Outline each blood parasite and name the species.
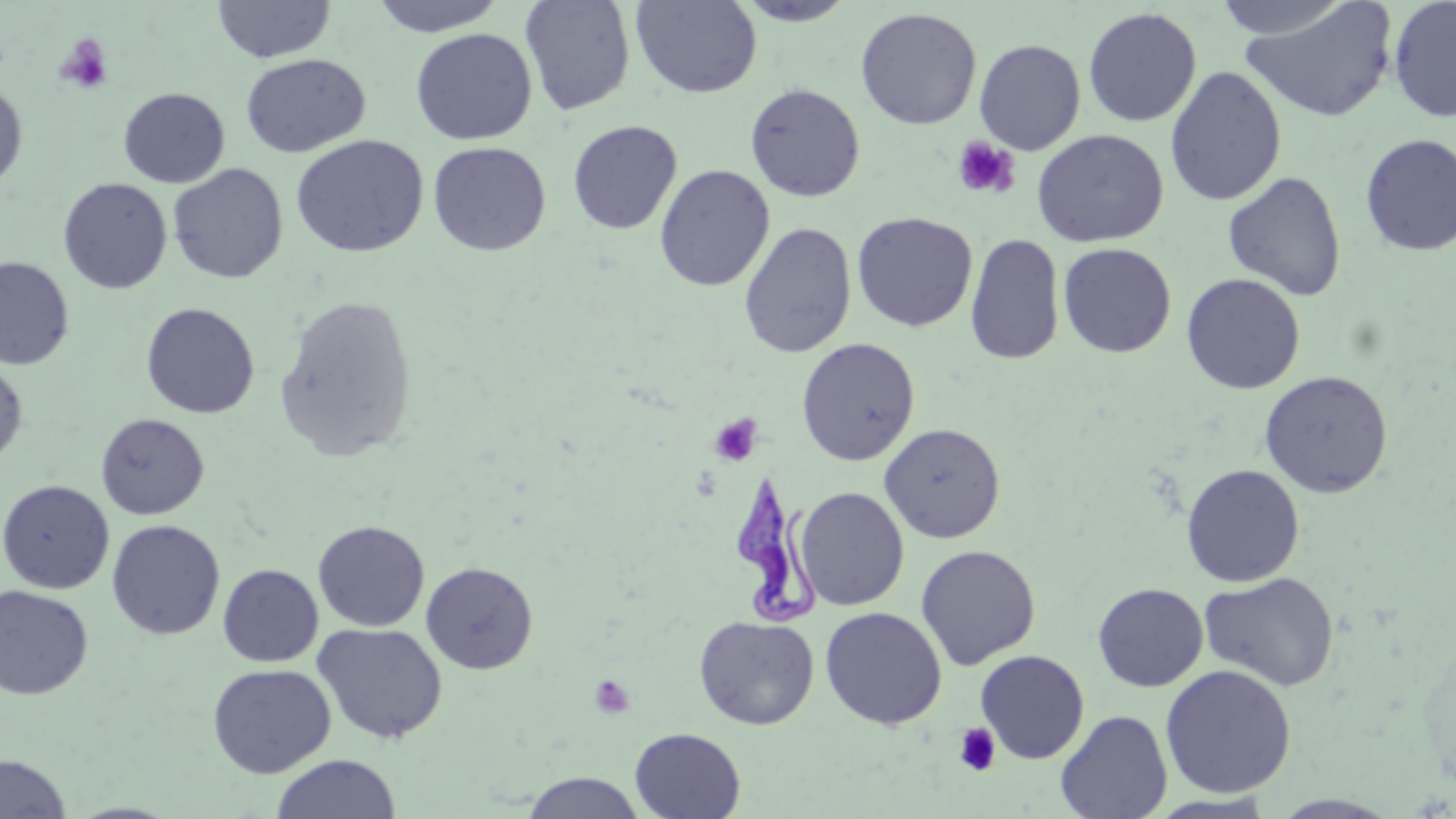
Approximate bounding boxes as (x1,y1)-(x2,y2) corner pairs in pixels.
Trypanosoma brucei: (725,475)-(826,628).
No Plasmodium falciparum, Plasmodium ovale, Plasmodium malariae, Plasmodium vivax, or Babesia divergens observed.

slide_level_diagnosis: Trypanosoma brucei
modality: light microscopy
platelet_locations: 'approximate bounding boxes as (x1,y1)-(x2,y2) corner pairs in pixels: (54,33)-(113,94), (951,136)-(1020,199), (709,414)-(762,466), (588,674)-(635,719), (953,723)-(1001,776)'
image_size: 1456×819 pixels
uninfected_red_blood_cell_locations: 'approximate bounding boxes as (x1,y1)-(x2,y2) corner pairs in pixels: (367,0)-(509,37), (519,0)-(637,116), (630,0)-(762,99), (1209,0)-(1356,41), (1387,0)-(1456,123), (212,1)-(335,63), (730,1)-(861,26), (1239,1)-(1399,123), (854,7)-(982,130), (1082,7)-(1202,127), (411,28)-(537,145), (974,39)-(1086,155), (240,53)-(370,158), (1165,65)-(1287,206), (0,80)-(28,193), (745,83)-(865,202), (118,87)-(230,188), (567,119)-(682,234), (1032,129)-(1168,248), (1359,133)-(1456,256), (290,135)-(429,258), (428,141)-(551,256), (167,163)-(288,284), (654,164)-(775,292), (1222,171)-(1347,302), (58,177)-(172,294), (852,211)-(978,332), (738,222)-(857,358), (867,229)-(1059,353), (965,232)-(1065,365), (1058,242)-(1176,358), (0,256)-(74,370), (1181,273)-(1306,395), (274,294)-(418,463), (140,302)-(260,419), (796,337)-(920,466), (0,356)-(28,469), (1259,370)-(1394,498), (95,413)-(209,520), (879,422)-(1006,543), (1181,464)-(1305,587), (0,479)-(114,594), (794,486)-(909,610), (106,519)-(225,641), (312,519)-(430,632), (916,544)-(1041,670), (420,560)-(539,675), (217,563)-(323,667), (1199,571)-(1339,692), (1092,582)-(1208,692), (0,585)-(94,700), (820,606)-(947,729), (694,614)-(820,730), (313,622)-(447,745), (974,650)-(1090,764), (207,663)-(336,778), (1160,664)-(1296,798), (1055,709)-(1173,819), (629,727)-(746,818), (0,753)-(72,818), (269,754)-(402,819), (522,772)-(646,818), (1146,792)-(1280,816), (1270,793)-(1402,817)'
field_of_view: one of a larger specimen
magnification: 1000x
preparation: thin blood smear
stain: May-Grünwald-Giemsa